Classify this cell by malaria status.
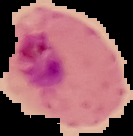
It is parasitized.

preparation = thin blood film
image size = 133×136 pixels
image type = segmented cell region with the area outside set to black